Classify this cell by malaria status.
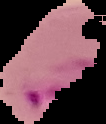
Parasitized.

Summary:
  - Preparation: thin blood smear
  - Image type: segmented cell region on a black background
  - Image size: 106×124 pixels